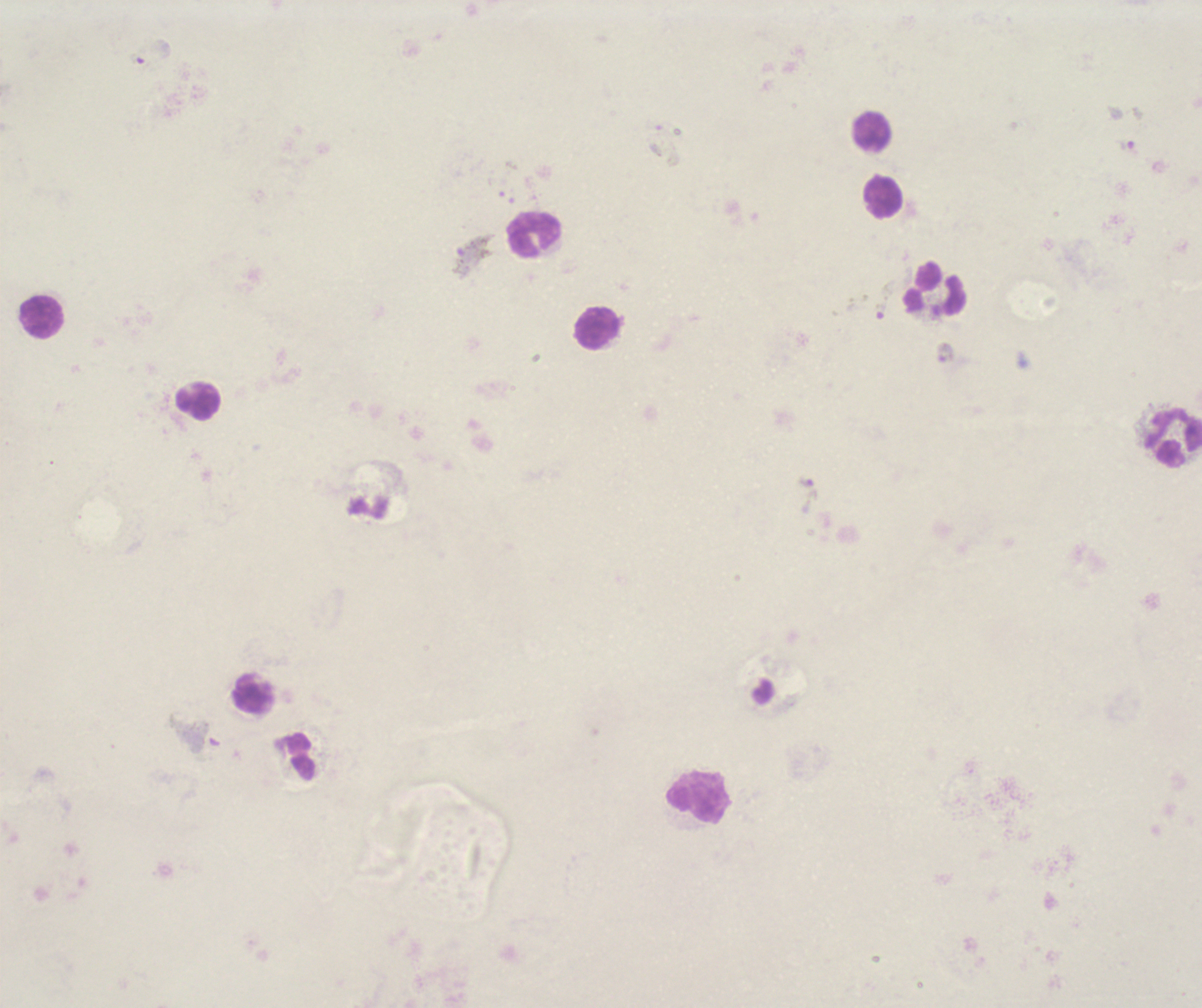

Approximate object centers, in pixels from the top-left corner. Gametocyte locations: (x=141, y=59), (x=472, y=254), (x=883, y=300), (x=808, y=495), (x=195, y=733). Leukocyte locations: (x=872, y=132), (x=885, y=198), (x=534, y=235), (x=936, y=290), (x=44, y=318), (x=596, y=329), (x=200, y=400), (x=1174, y=437), (x=253, y=694), (x=698, y=797). Thick blood smear. One field from this slide. Captured at 100x magnification. Romanowsky stain. Background quality: poor. Previously used in an actual diagnosis. Result: positive for malaria parasites. Image is 1202×1008 pixels. Coloration quality: bad.